Locate every Plasmodium parasite.
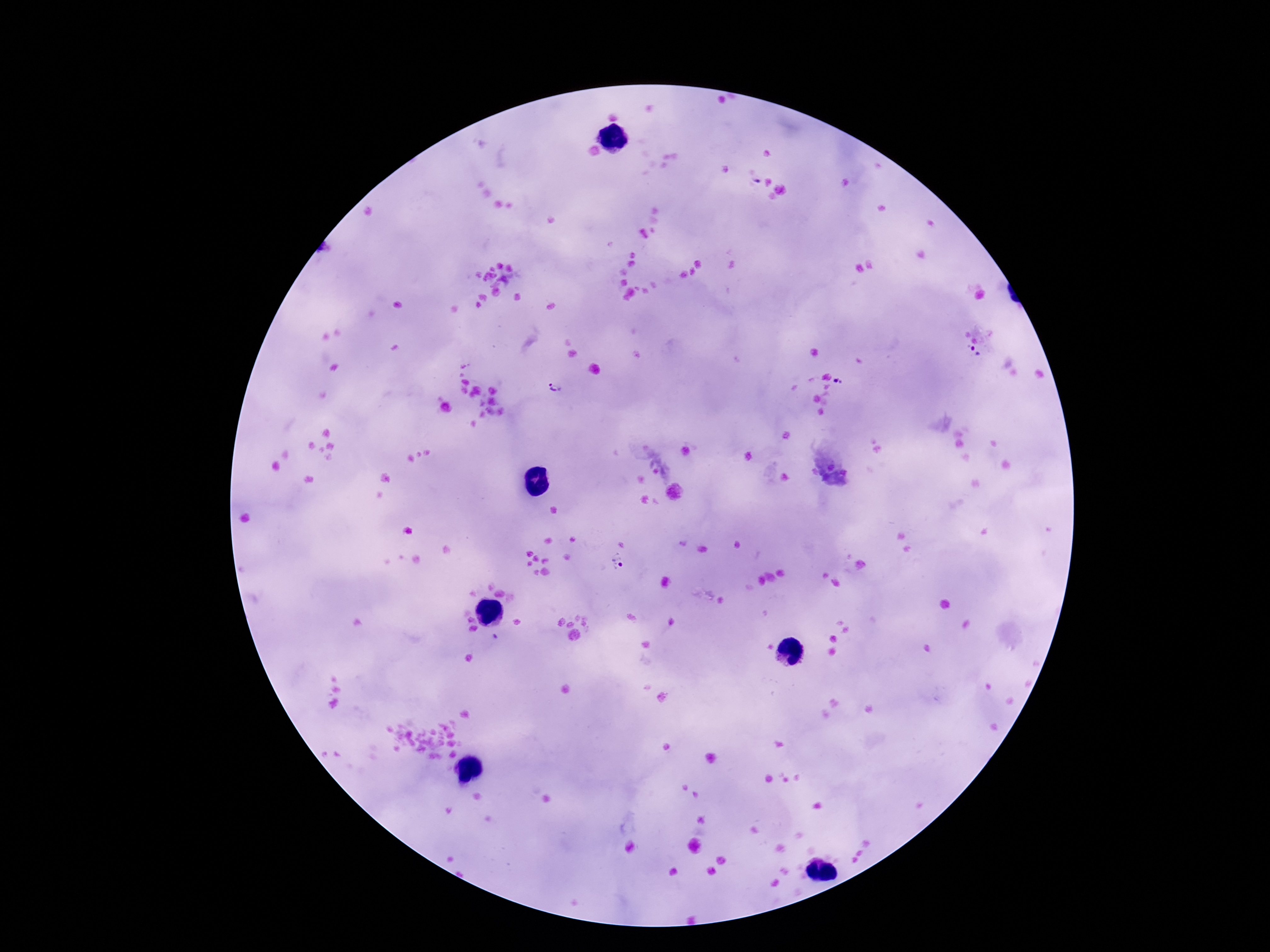
Approximate centers as (x, y) in pixels.
Plasmodium parasites: (974, 354), (837, 381), (555, 390), (618, 562).

Summary:
  - Image size: 1270×952 pixels
  - Capture: smartphone camera through the microscope eyepiece
  - Stain: Giemsa
  - Preparation: thick blood smear
  - Patient malaria status: infected
  - Magnification: 100x
  - Field of view: single